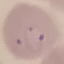
Result: malaria parasites identified. Thin blood film. Automatically extracted cell patch, resized to 64 × 64 pixels. Photographed with a smartphone camera at the microscope eyepiece. Giemsa stain.